Report the malaria status of this cell.
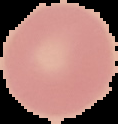
It is uninfected.

The area outside the segmented cell region is set to black. From a thin blood smear. Image is 118×124 pixels.